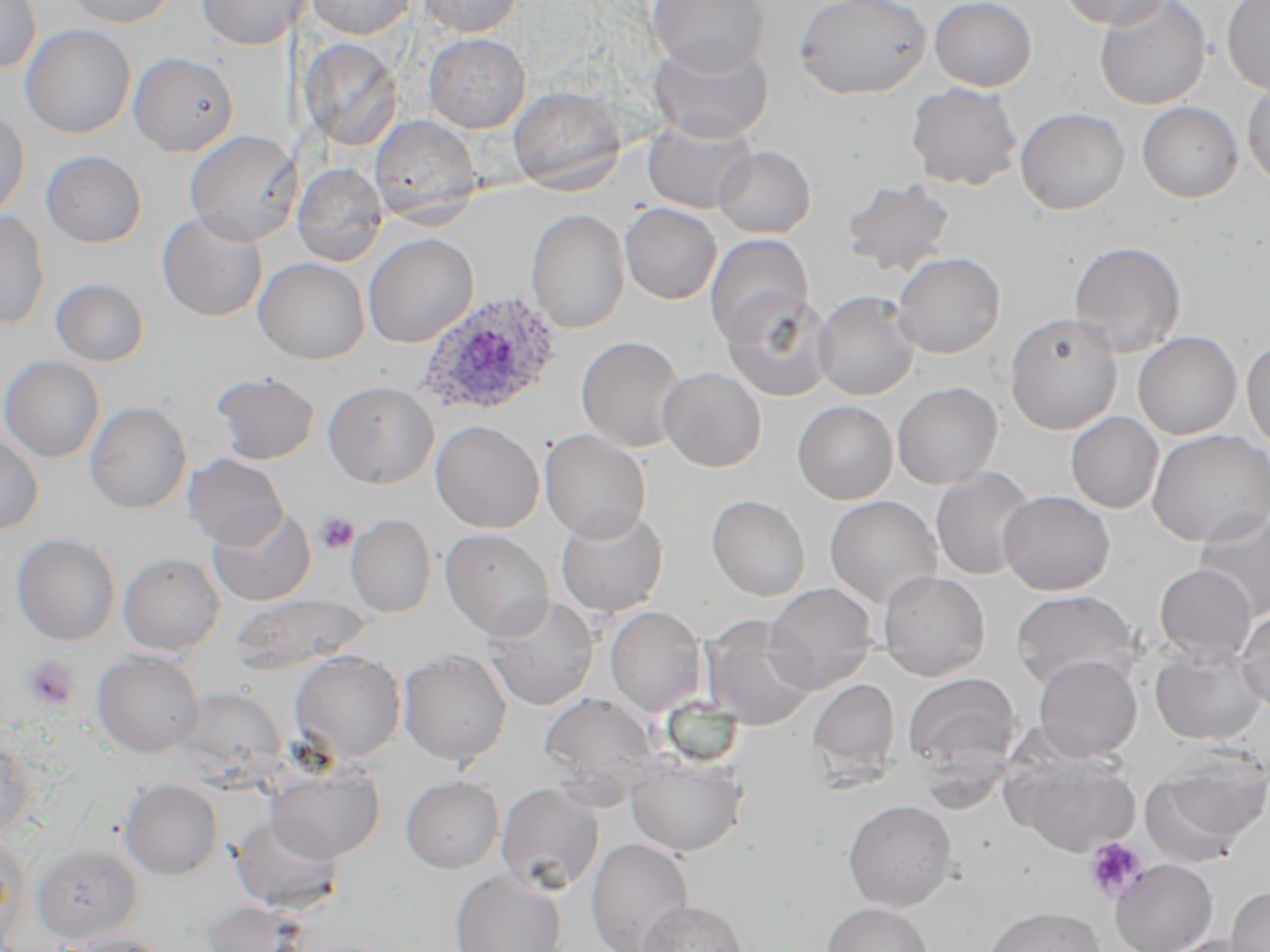

Approximate bounding boxes as (x1, y1, x2, y2) in pixels. Platelet locations: (316, 512, 358, 554), (23, 655, 79, 711), (1084, 836, 1149, 903). Uninfected red blood cell locations: (0, 0, 42, 73), (63, 0, 177, 28), (196, 0, 309, 51), (304, 0, 417, 39), (417, 0, 522, 36), (646, 0, 770, 74), (794, 0, 933, 100), (929, 0, 1037, 91), (1057, 0, 1173, 30), (1093, 0, 1211, 110), (1221, 0, 1270, 94), (20, 24, 136, 138), (423, 33, 531, 133), (649, 37, 774, 143), (298, 39, 404, 151), (128, 51, 239, 156), (1242, 77, 1270, 192), (905, 82, 1023, 191), (508, 86, 626, 192), (1137, 102, 1243, 203), (0, 105, 30, 220), (1014, 107, 1130, 215), (369, 115, 482, 226), (643, 118, 759, 214), (184, 130, 300, 244), (713, 146, 816, 239), (41, 150, 147, 248), (293, 164, 388, 267), (840, 178, 956, 277), (620, 203, 722, 304), (526, 209, 630, 333), (0, 211, 51, 330), (157, 211, 268, 322), (363, 233, 479, 348), (704, 233, 814, 345), (1068, 240, 1187, 357), (891, 251, 1006, 358), (253, 257, 370, 365), (50, 278, 150, 367), (813, 291, 920, 400), (722, 292, 835, 403), (1004, 312, 1123, 435), (1133, 331, 1242, 439), (576, 336, 686, 453), (1241, 338, 1270, 454), (0, 355, 105, 463), (658, 367, 766, 472), (210, 371, 320, 465), (323, 380, 439, 489), (891, 381, 1003, 490), (85, 401, 192, 514), (792, 401, 898, 505), (1065, 411, 1164, 514), (430, 420, 544, 533), (1146, 428, 1270, 547), (540, 430, 651, 542), (0, 433, 45, 536), (183, 453, 288, 549), (930, 467, 1037, 581), (998, 490, 1115, 595), (706, 495, 810, 601), (824, 495, 943, 610), (207, 505, 316, 607), (555, 506, 669, 617), (1193, 508, 1270, 620), (346, 514, 436, 617), (439, 528, 554, 639), (11, 533, 121, 646), (118, 551, 226, 656), (1153, 563, 1257, 663), (878, 570, 990, 681), (763, 582, 879, 694), (1011, 590, 1140, 692), (229, 593, 375, 674), (484, 594, 598, 711), (605, 606, 707, 716), (1237, 608, 1270, 717), (699, 615, 818, 731), (1149, 646, 1268, 746), (398, 648, 512, 766), (92, 649, 207, 758), (289, 650, 407, 763), (1033, 655, 1142, 761), (902, 671, 1022, 780), (806, 678, 901, 781), (538, 692, 659, 805), (0, 734, 37, 844), (1005, 748, 1142, 858), (625, 751, 748, 857), (1140, 753, 1269, 866), (267, 765, 386, 862), (400, 775, 504, 874), (121, 779, 224, 880), (496, 781, 605, 894), (842, 799, 958, 911), (230, 813, 342, 912), (586, 837, 695, 951), (32, 845, 143, 943), (1110, 859, 1218, 952), (449, 869, 567, 952), (1226, 886, 1270, 952), (199, 899, 308, 952), (637, 899, 747, 952), (821, 902, 933, 952), (984, 905, 1105, 952), (62, 932, 173, 952), (1155, 935, 1264, 952). Plasmodium ovale-infected red blood cell locations: (416, 290, 565, 418). Slide-level diagnosis: Plasmodium ovale. Optical microscopy. Thin blood film. 1000x magnification. May-Grünwald-Giemsa stain. Image is 1270×952 pixels. One field of a larger specimen.